Locate every leukocyte (white blood cell).
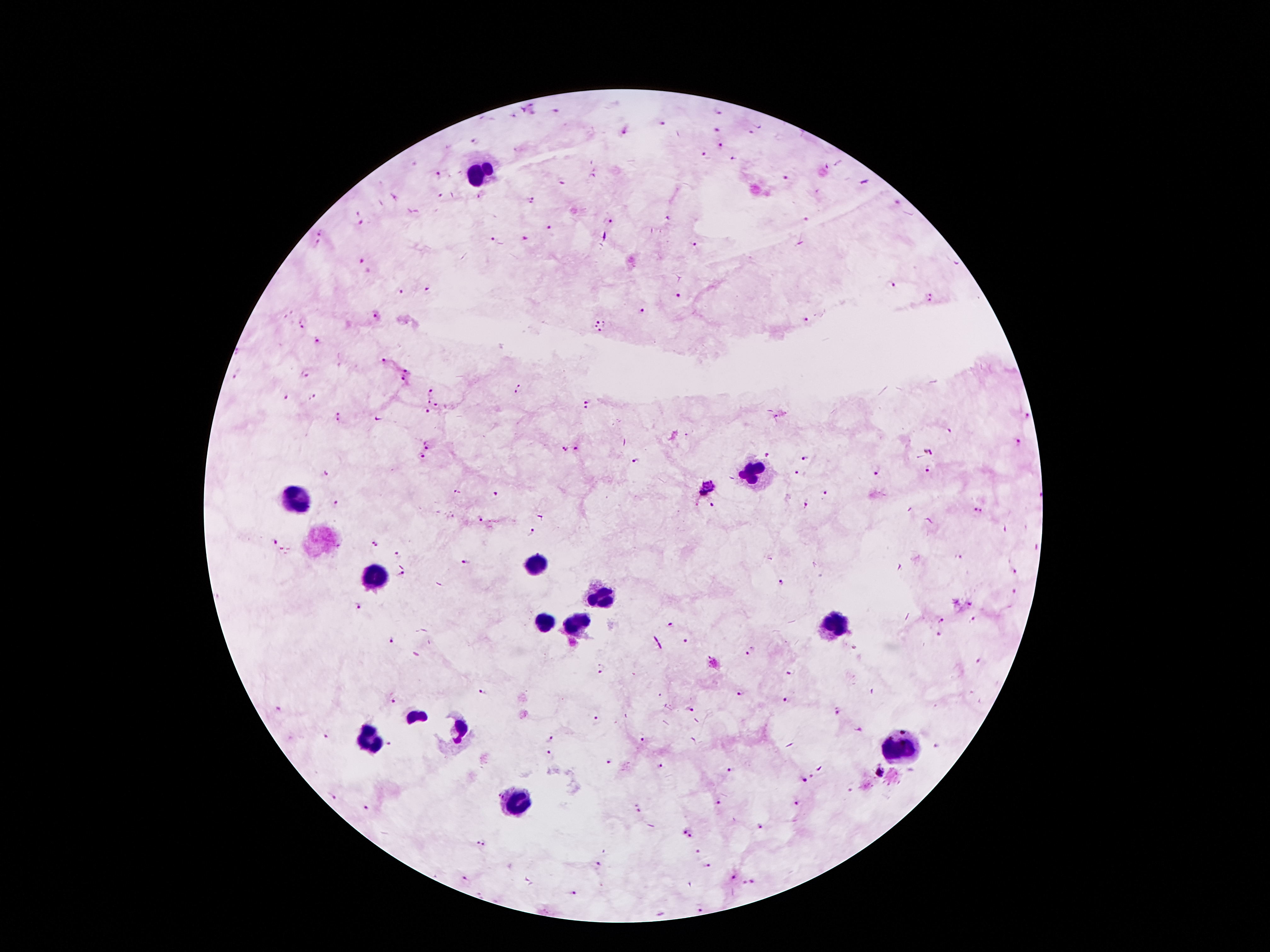
Approximate centers as (x, y) in pixels.
Leukocytes: (479, 170), (752, 472), (296, 501), (533, 564), (378, 576), (603, 600), (575, 621), (546, 623), (836, 623), (370, 742), (901, 751), (514, 802).

Plasmodium parasite locations: (663, 123), (717, 130), (625, 131), (751, 131), (476, 143), (719, 145), (705, 155), (735, 159), (438, 175), (787, 179), (562, 182), (440, 195), (531, 202), (609, 222), (363, 223), (551, 228), (321, 232), (525, 238), (492, 239), (318, 243), (695, 244), (361, 263), (890, 286), (428, 288), (401, 290), (679, 296), (929, 297), (642, 309), (377, 317), (806, 319), (301, 324), (601, 326), (318, 340), (384, 360), (406, 372), (237, 375), (303, 375), (405, 379), (518, 390), (432, 392), (285, 398), (313, 398), (431, 402), (438, 404), (585, 405), (426, 412), (1025, 416), (339, 418), (378, 419), (949, 431), (689, 434), (1017, 443), (428, 445), (564, 448), (576, 448), (928, 452), (423, 455), (767, 456), (805, 460), (636, 461), (927, 470), (797, 471), (877, 473), (326, 475), (707, 489), (458, 493), (824, 493), (495, 495), (1039, 495), (336, 503), (805, 503), (713, 506), (980, 511), (479, 518), (533, 532), (275, 541), (373, 544), (397, 554), (961, 557), (465, 562), (1014, 572), (402, 574), (781, 582), (1014, 589), (971, 604), (357, 605), (973, 619), (941, 620), (670, 622), (939, 633), (391, 640), (686, 640), (752, 650), (980, 660), (603, 669), (791, 672), (483, 691), (742, 694), (658, 695), (394, 700), (787, 700), (688, 708), (836, 711), (597, 720), (327, 736), (550, 739), (642, 740), (389, 746), (936, 747), (549, 753), (611, 760), (659, 766), (733, 770), (880, 771), (816, 778), (803, 781), (333, 795), (719, 801), (797, 802), (366, 807), (637, 808), (760, 825), (687, 834), (480, 843), (697, 852), (598, 865), (707, 866), (733, 877), (466, 880), (749, 882), (572, 893), (700, 908). Smartphone photograph taken through the microscope eyepiece. 100x magnification. Thick blood film. Image is 1270×952 pixels. Patient malaria status: infected with Plasmodium falciparum. One field from this slide. Giemsa-stained preparation.